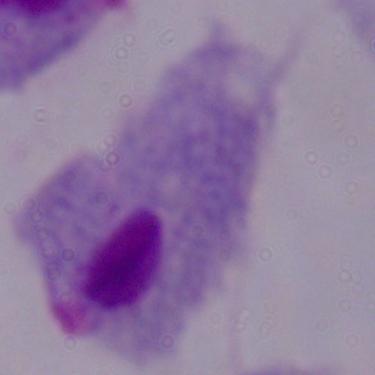

{
  "identification": "trichomonad",
  "modality": "photomicrograph",
  "magnification": "1000x"
}